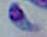
Micrograph. Toxoplasma gondii is seen. Captured at 1000x magnification.